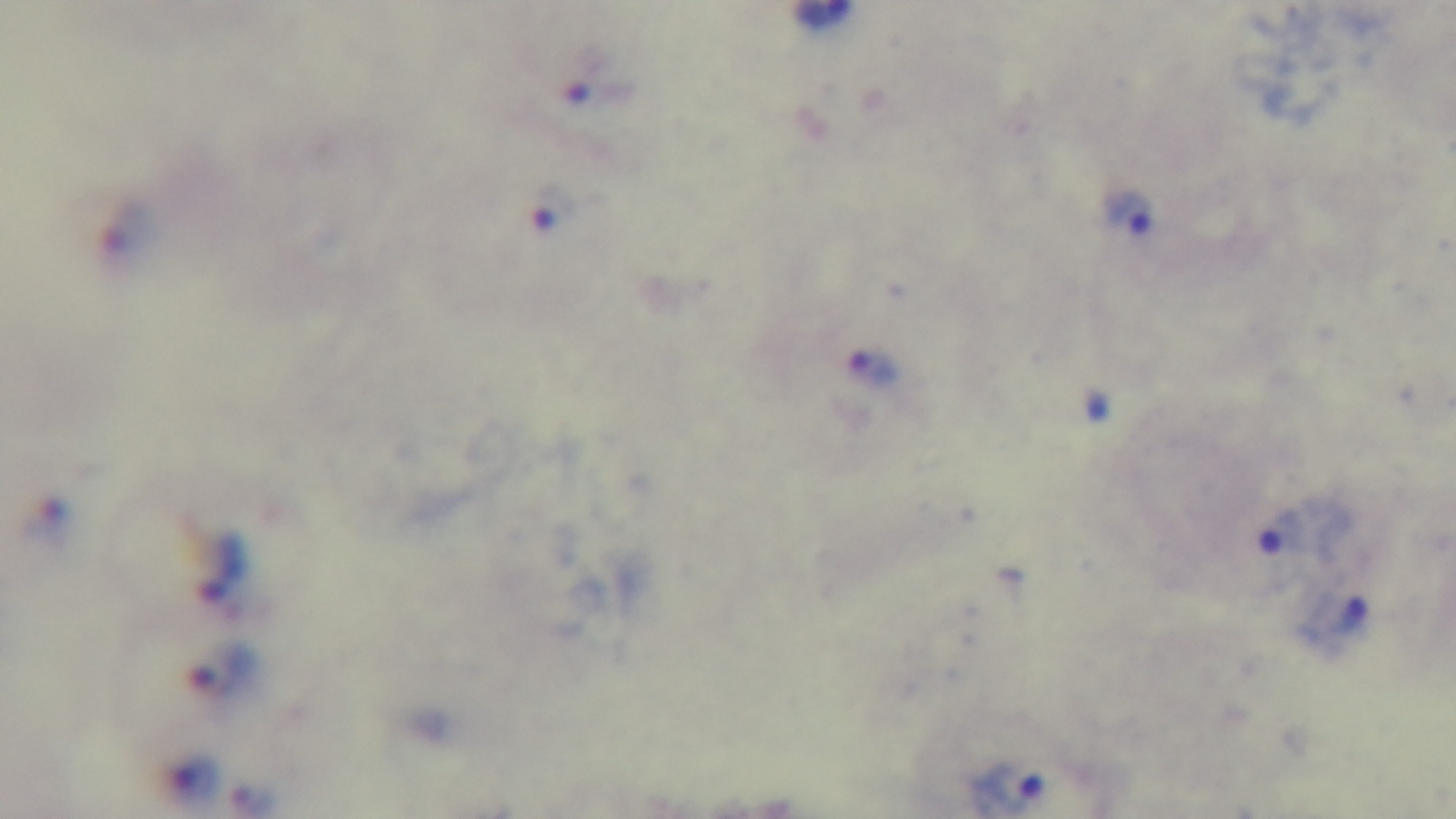

Summary:
  - Malaria status: infected
  - Capture: mounted 4K digital camera
  - Stain: Giemsa
  - Preparation: thick
  - Field of view: single
  - Modality: light microscopy
  - Objective: 100x oil immersion